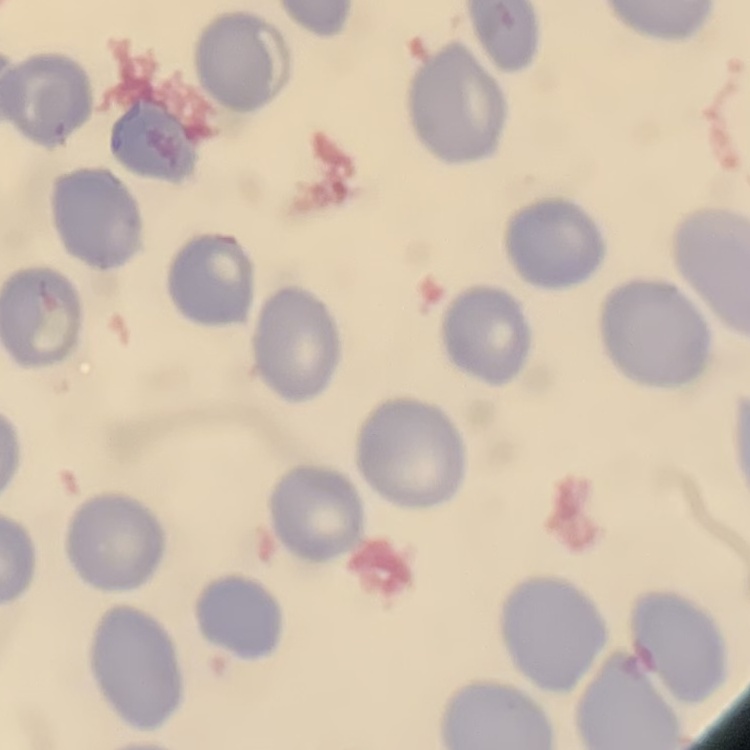
Summary:
  - Erythrocyte morphology: no rouleaux formation
  - Preparation: thin peripheral smear
  - Image type: square crop of a larger photomicrograph
  - Stain: Field's or Giemsa